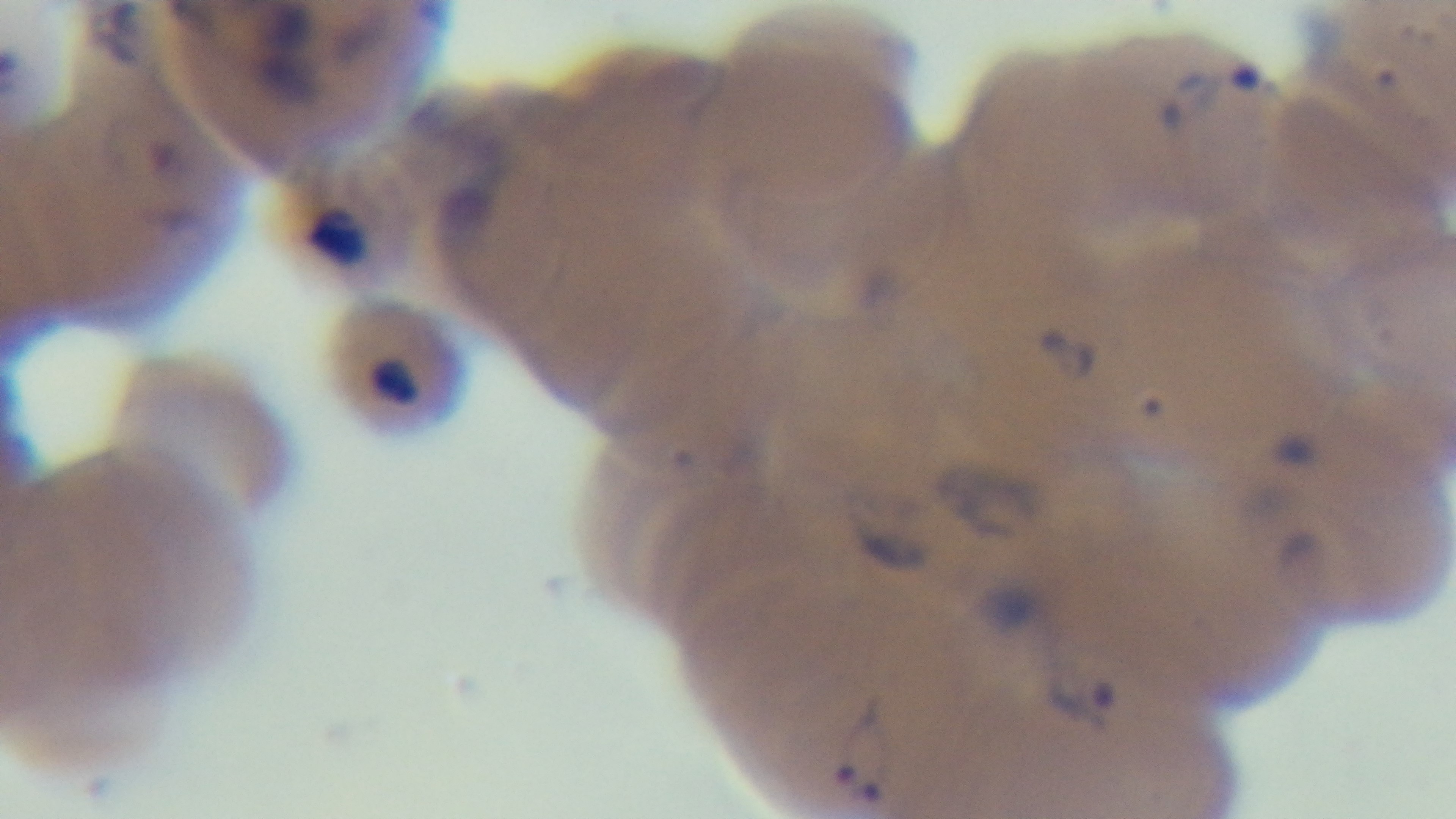

{
  "capture": "mounted 4K digital camera",
  "modality": "light microscopy",
  "malaria_status": "positive",
  "field_of_view": "one from the slide",
  "objective": "100x oil immersion",
  "stain": "Giemsa",
  "preparation": "thin smear"
}